Report the malaria status of this cell.
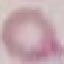
It is uninfected.

stain = Giemsa
capture = smartphone through the microscope eyepiece
image type = cell patch, automatically extracted from a larger field of view and resized to 64 × 64 pixels
preparation = thin blood film